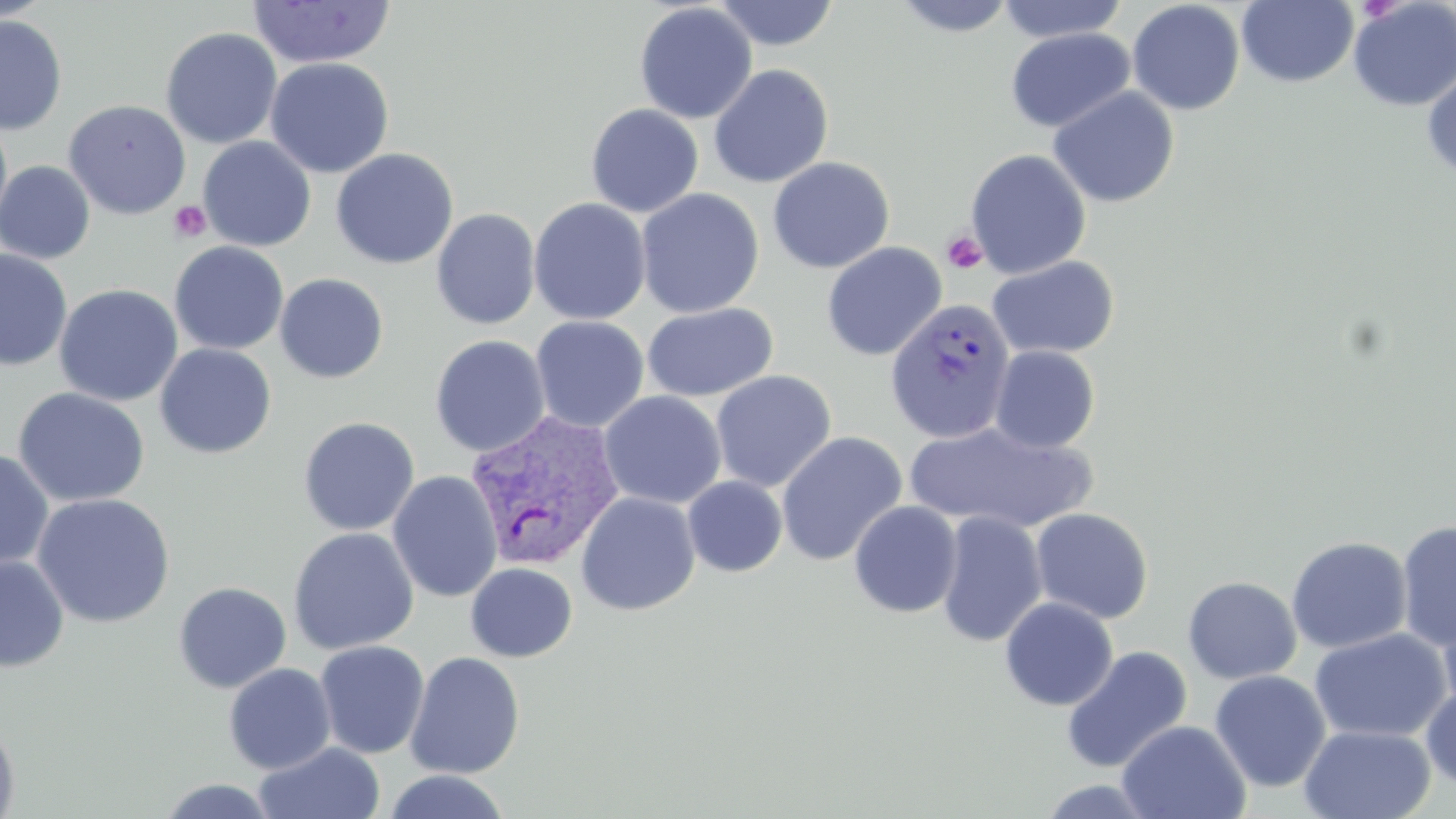
slide_level_diagnosis: Plasmodium vivax
preparation: thin blood film
platelet_locations: 'approximate bounding boxes as (x1, y1, x2, y2) in pixels: (168, 200, 212, 243), (941, 230, 989, 274)'
modality: optical microscopy
field_of_view: single
image_size: 1456×819 pixels
magnification: 1000x
plasmodium_vivax_infected_red_blood_cell_locations: 'approximate bounding boxes as (x1, y1, x2, y2) in pixels: (885, 298, 1016, 444), (463, 410, 626, 573)'
stain: May-Grünwald-Giemsa
uninfected_red_blood_cell_locations: 'approximate bounding boxes as (x1, y1, x2, y2) in pixels: (0, 0, 53, 22), (893, 0, 1017, 37), (996, 0, 1130, 44), (1348, 0, 1456, 111), (248, 1, 395, 69), (712, 1, 841, 51), (1127, 1, 1245, 115), (1236, 1, 1359, 88), (634, 3, 757, 124), (0, 14, 67, 135), (160, 27, 283, 149), (1005, 28, 1135, 133), (265, 57, 394, 178), (708, 64, 834, 189), (1421, 65, 1456, 183), (1047, 87, 1180, 208), (63, 99, 191, 220), (585, 104, 704, 218), (0, 113, 13, 235), (198, 136, 316, 252), (196, 143, 453, 254), (331, 148, 458, 270), (965, 148, 1091, 278), (767, 156, 895, 274), (0, 160, 96, 264), (635, 188, 764, 318), (528, 198, 651, 325), (430, 208, 541, 329), (170, 241, 289, 355), (821, 242, 947, 361), (0, 248, 73, 371), (987, 255, 1119, 360), (275, 273, 388, 384), (53, 284, 183, 407), (642, 302, 778, 401), (530, 316, 649, 433), (429, 334, 550, 457), (154, 343, 276, 459), (990, 345, 1100, 453), (710, 370, 837, 492), (13, 387, 150, 507), (598, 391, 727, 509), (298, 416, 420, 536), (904, 422, 1096, 534), (776, 432, 907, 566), (0, 448, 54, 571), (928, 458, 1084, 622), (388, 470, 503, 603), (683, 476, 788, 577), (575, 492, 701, 616), (32, 493, 175, 628), (848, 501, 963, 618), (1030, 508, 1154, 624), (936, 512, 1047, 647), (1396, 519, 1456, 652), (288, 527, 419, 655), (1286, 535, 1412, 653), (0, 555, 69, 673), (465, 562, 577, 662), (1182, 575, 1302, 685), (172, 581, 292, 693), (999, 597, 1119, 710), (1437, 598, 1456, 717), (1310, 627, 1451, 742), (314, 640, 430, 759), (1061, 646, 1193, 774), (405, 651, 525, 779), (223, 662, 336, 774), (1209, 670, 1331, 792), (1421, 683, 1456, 790), (0, 717, 21, 818), (1116, 720, 1251, 819), (1299, 724, 1436, 819), (254, 742, 386, 819), (382, 770, 512, 819), (1035, 777, 1159, 818), (156, 778, 282, 818)'